Point out each Plasmodium parasite and each leukocyte.
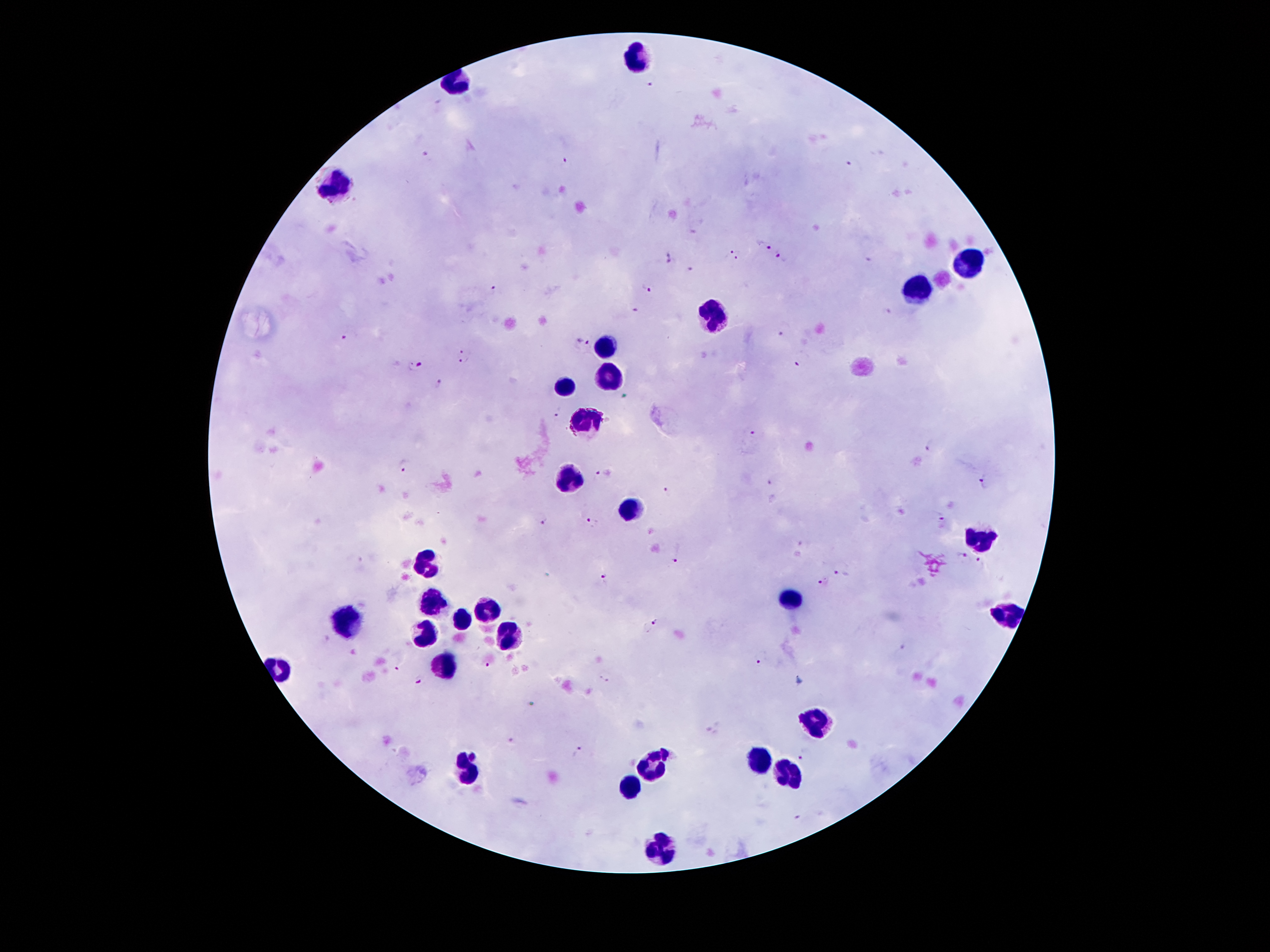
Approximate centers as (x, y) in pixels.
Plasmodium parasites: (649, 84), (425, 155), (565, 159), (849, 163), (693, 230), (765, 246), (732, 251), (668, 253), (781, 257), (738, 258), (868, 258), (669, 263), (690, 269), (646, 286), (493, 289), (636, 309), (888, 310), (781, 333), (345, 338), (582, 342), (467, 351), (462, 362), (420, 365), (796, 366), (440, 383), (559, 413), (752, 432), (932, 447), (404, 464), (604, 473), (769, 481), (985, 481), (665, 492), (940, 517), (544, 522), (591, 522), (806, 545), (963, 555), (676, 560), (979, 560), (841, 572), (605, 578), (821, 584), (656, 623), (329, 640), (904, 645), (351, 653), (759, 663), (489, 666), (397, 667), (604, 677), (421, 682), (512, 739), (577, 751), (803, 757), (797, 816).
Leukocytes: (639, 60), (454, 86), (338, 187), (965, 263), (917, 293), (715, 314), (605, 345), (611, 375), (568, 386), (586, 427), (570, 481), (979, 539), (426, 565), (431, 601), (790, 601), (486, 608), (1010, 613), (461, 619), (345, 623), (424, 635), (508, 638), (450, 663), (814, 724), (758, 762), (652, 766), (469, 771), (790, 778), (631, 788), (665, 847).

capture = smartphone through the microscope eyepiece
magnification = 100x
preparation = thick blood film
stain = Giemsa
patient malaria status = positive for Plasmodium falciparum
image size = 1270×952 pixels
field of view = single